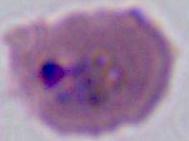

Summary:
  - Magnification: 400x or 1000x
  - Modality: photomicrograph
  - Identification: Plasmodium